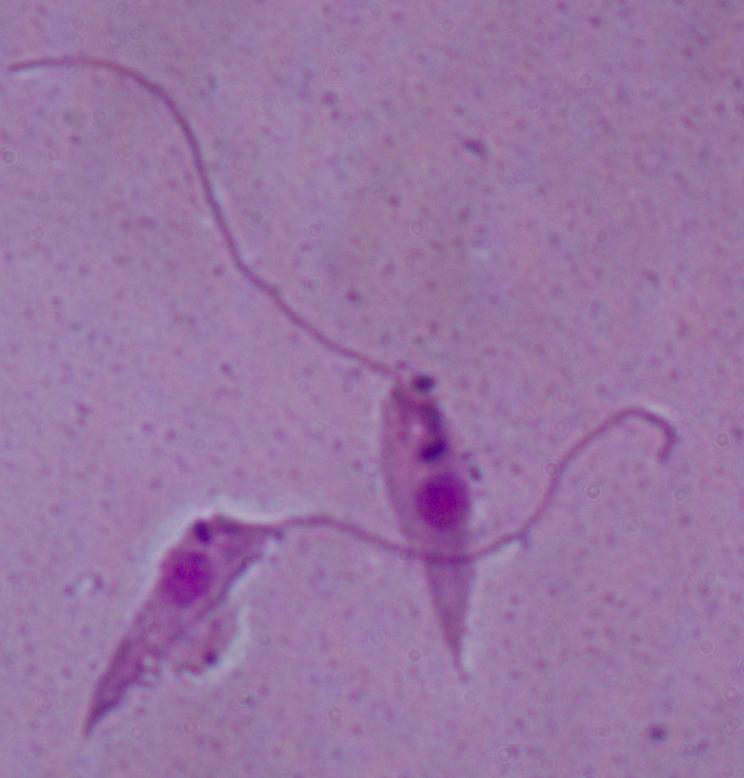

A Leishmania parasite is seen. 1000x magnification. Micrograph.